Mark where platelets are.
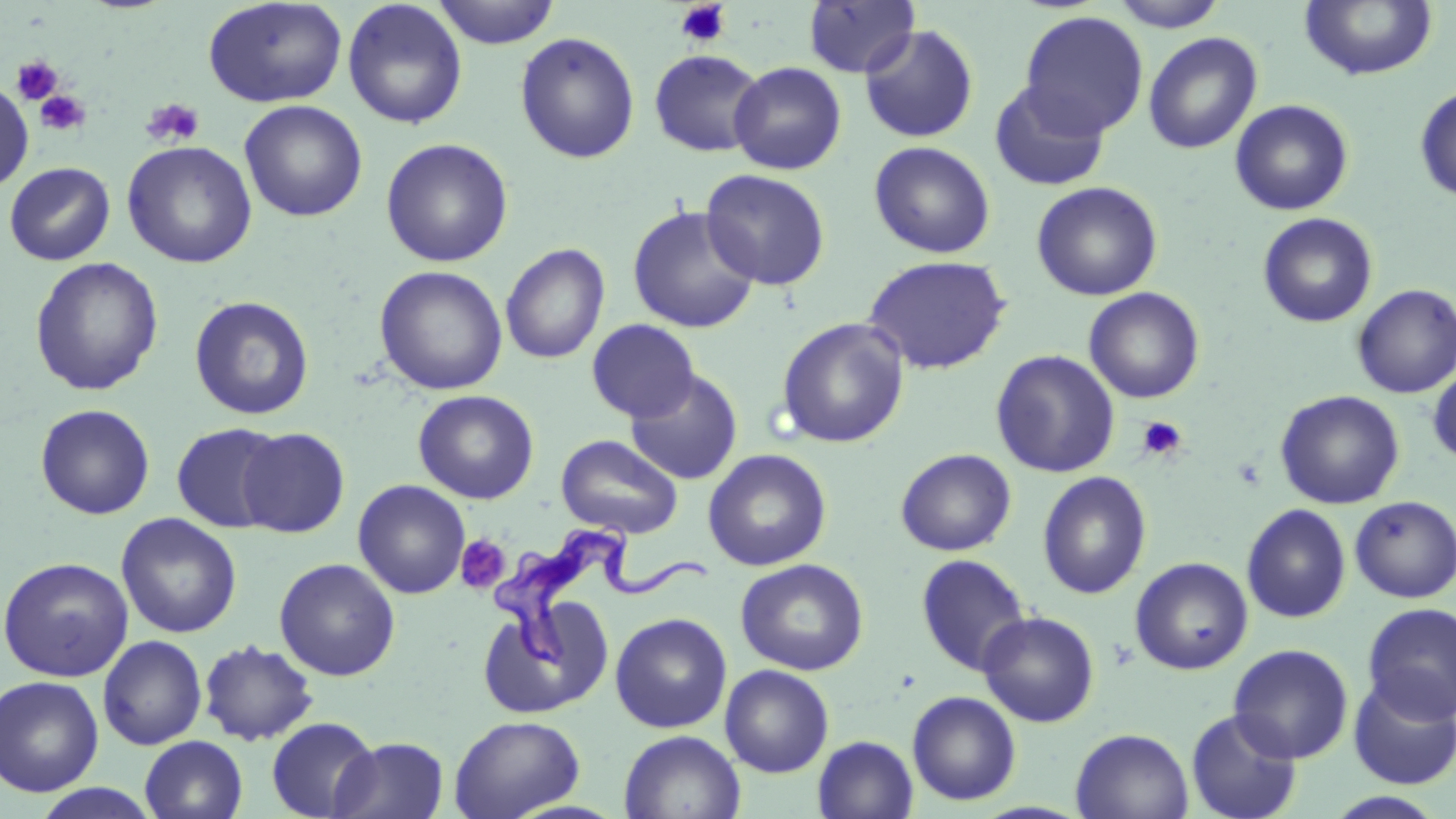

Approximate bounding boxes as [x1, y1, x2, y2] in pixels.
Platelets: [674, 1, 731, 48], [11, 56, 63, 105], [35, 91, 91, 137], [140, 97, 204, 148], [1136, 415, 1188, 462], [455, 535, 510, 593].

slide-level diagnosis = Trypanosoma brucei
modality = light microscopy
uninfected red blood cell locations = approximate bounding boxes as [x1, y1, x2, y2] in pixels: [202, 0, 348, 108], [432, 0, 561, 48], [1109, 0, 1228, 31], [342, 1, 467, 129], [803, 1, 920, 79], [1299, 1, 1438, 81], [1019, 10, 1149, 139], [858, 24, 980, 143], [515, 31, 640, 164], [1143, 32, 1263, 154], [648, 49, 765, 157], [729, 61, 847, 175], [0, 79, 34, 194], [988, 81, 1110, 192], [1414, 84, 1456, 202], [1229, 99, 1353, 215], [239, 100, 368, 222], [380, 137, 513, 267], [122, 140, 257, 268], [869, 140, 996, 258], [3, 161, 116, 266], [701, 168, 831, 290], [1031, 181, 1163, 301], [626, 205, 761, 334], [1257, 212, 1378, 328], [500, 243, 610, 364], [862, 254, 1012, 375], [29, 256, 164, 396], [374, 265, 508, 396], [1352, 283, 1456, 399], [1083, 287, 1205, 403], [189, 295, 314, 420], [775, 317, 910, 449], [586, 319, 699, 422], [990, 349, 1121, 478], [1427, 362, 1456, 466], [626, 369, 743, 485], [1275, 389, 1405, 509], [413, 390, 539, 504], [35, 404, 155, 520], [171, 422, 286, 533], [237, 426, 350, 538], [556, 434, 683, 539], [895, 447, 1016, 556], [702, 448, 832, 571], [1037, 470, 1152, 599], [352, 479, 470, 599], [1350, 496, 1456, 603], [1242, 504, 1351, 623], [115, 512, 241, 639], [916, 552, 1033, 676], [0, 556, 134, 682], [274, 557, 401, 681], [1130, 557, 1253, 675], [735, 558, 869, 676], [477, 596, 613, 719], [1361, 602, 1456, 723], [977, 611, 1100, 728], [610, 612, 732, 733], [97, 635, 207, 750], [199, 639, 319, 747], [1228, 643, 1353, 763], [720, 664, 834, 777], [0, 675, 104, 797], [1348, 675, 1456, 790], [907, 690, 1022, 806], [1185, 708, 1303, 819], [449, 715, 585, 819], [266, 716, 380, 818], [1071, 728, 1194, 819], [618, 729, 746, 818], [140, 735, 248, 819], [812, 735, 919, 818], [331, 736, 449, 819], [30, 784, 162, 818], [1322, 791, 1448, 819]
Trypanosoma brucei locations = approximate bounding boxes as [x1, y1, x2, y2] in pixels: [487, 516, 713, 671]
field of view = one of a larger specimen
stain = May-Grünwald-Giemsa
image size = 1456×819 pixels
preparation = thin blood smear
magnification = 1000x